Point out each malaria parasite and each leukocyte.
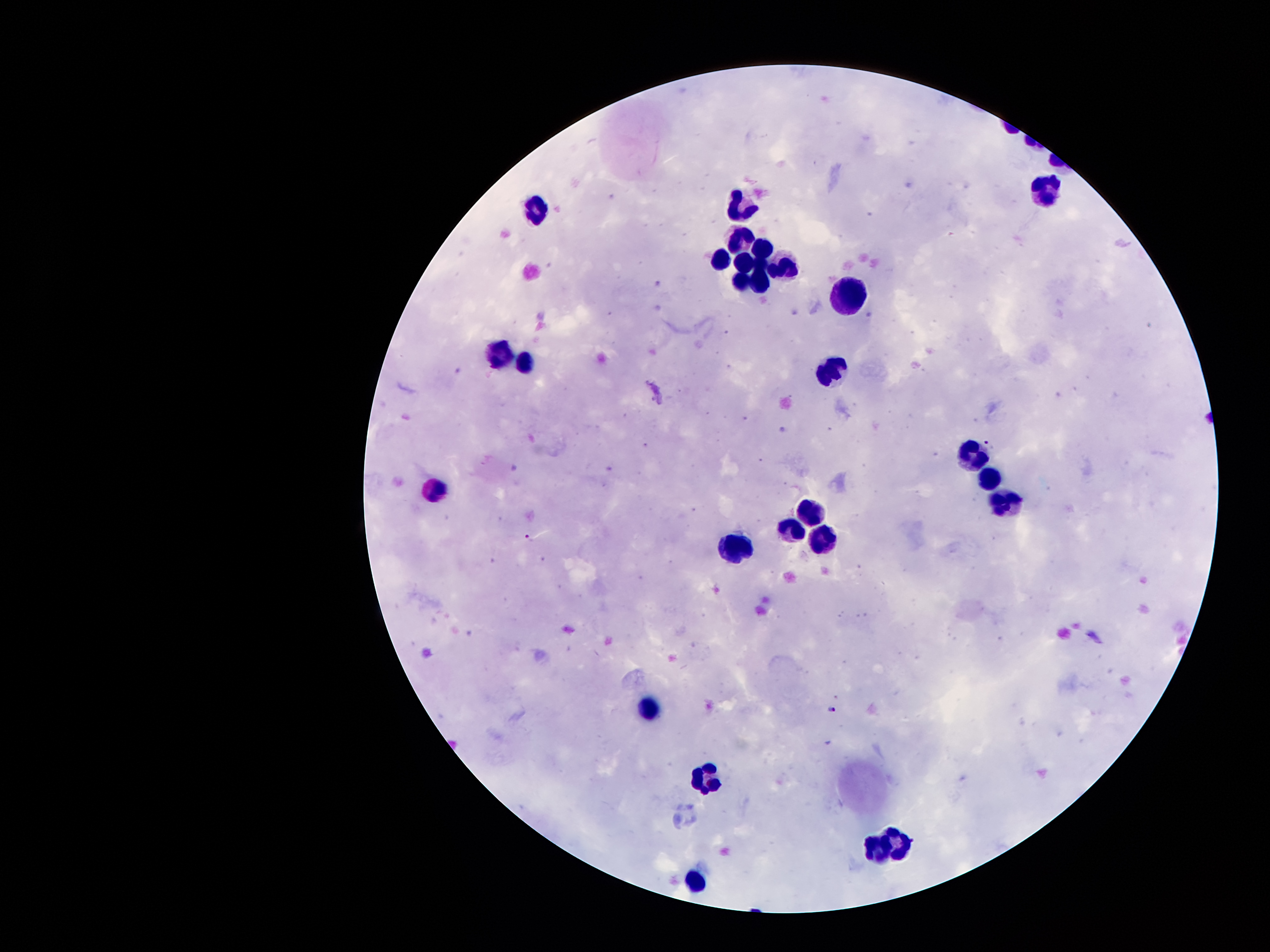

Approximate object centers, in pixels from the top-left corner.
Malaria parasites: (x=990, y=445), (x=530, y=540), (x=833, y=710).
Leukocytes: (x=1040, y=186), (x=743, y=207), (x=536, y=208), (x=740, y=237), (x=761, y=249), (x=738, y=255), (x=716, y=257), (x=780, y=265), (x=756, y=266), (x=737, y=278), (x=754, y=284), (x=847, y=289), (x=501, y=347), (x=523, y=355), (x=829, y=368), (x=968, y=455), (x=987, y=478), (x=431, y=488), (x=1003, y=501), (x=808, y=509), (x=790, y=528), (x=827, y=539), (x=732, y=549), (x=646, y=712), (x=708, y=775), (x=905, y=843), (x=869, y=851), (x=693, y=880).

Summary:
  - Magnification: 100x
  - Image size: 1270×952 pixels
  - Capture: smartphone through the microscope eyepiece
  - Stain: Giemsa
  - Field of view: single
  - Preparation: thick blood smear
  - Patient malaria status: positive for Plasmodium falciparum